Locate and identify every blood parasite.
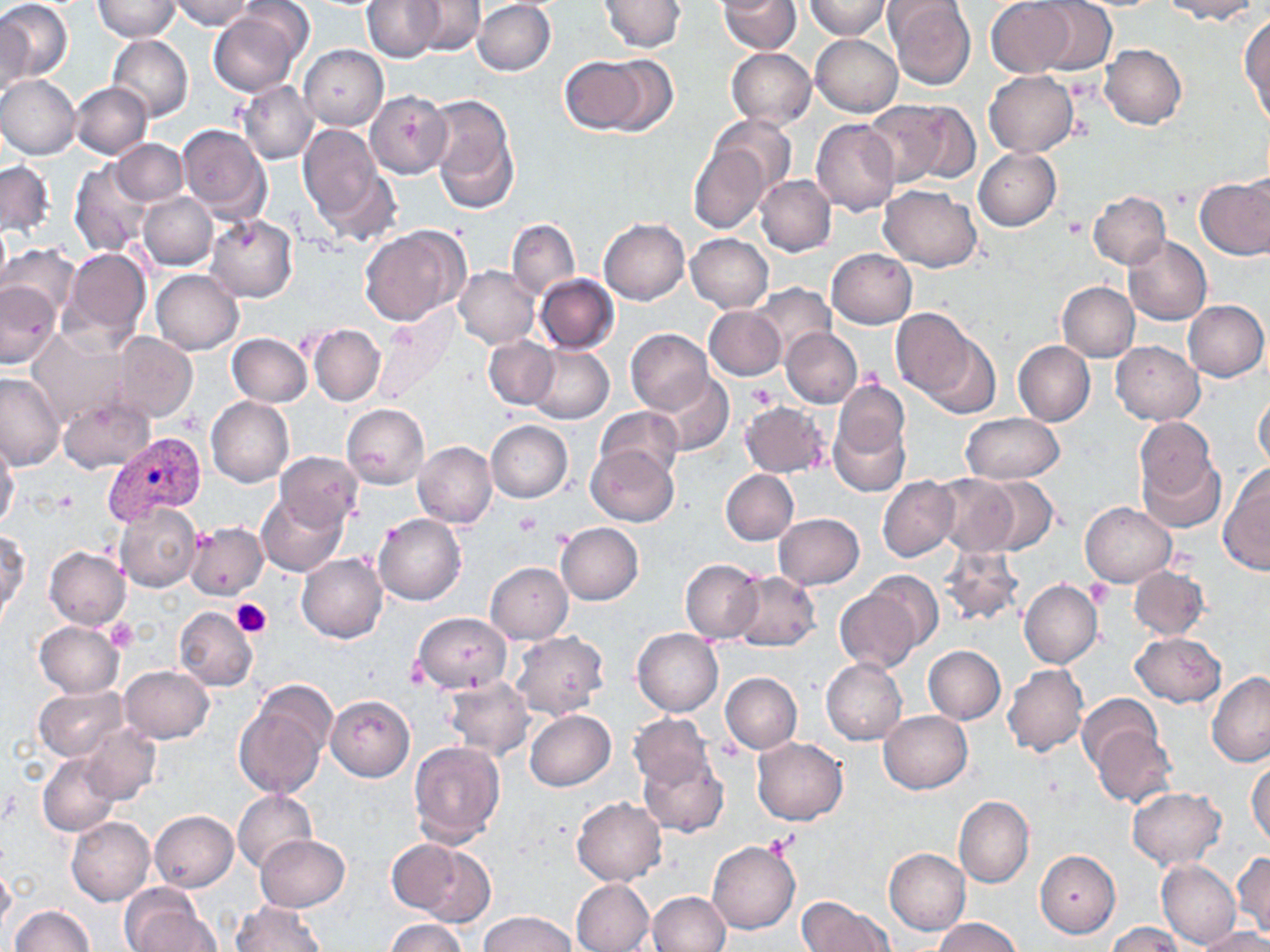
Approximate bounding boxes as [x1, y1, x2, y2] in pixels.
Plasmodium vivax-infected red blood cells: [102, 433, 207, 524].
No Plasmodium falciparum, Plasmodium ovale, Plasmodium malariae, Babesia divergens, or Trypanosoma brucei observed.

Platelet locations: [1063, 215, 1086, 238], [856, 364, 882, 389], [749, 385, 779, 412], [513, 511, 540, 536], [1085, 580, 1114, 608], [231, 597, 271, 638], [104, 619, 138, 652]. Uninfected red blood cell locations: [0, 0, 72, 82], [169, 0, 253, 30], [362, 0, 443, 61], [409, 0, 483, 56], [598, 0, 685, 52], [716, 0, 801, 53], [804, 0, 890, 39], [885, 0, 976, 90], [1163, 0, 1260, 22], [94, 1, 179, 41], [472, 1, 556, 76], [1028, 1, 1116, 73], [986, 2, 1078, 77], [589, 9, 684, 93], [0, 10, 35, 102], [209, 10, 304, 97], [1240, 16, 1269, 120], [107, 34, 193, 122], [811, 34, 902, 117], [298, 44, 388, 130], [1100, 44, 1187, 129], [726, 48, 816, 128], [596, 54, 678, 138], [559, 56, 652, 134], [984, 71, 1079, 156], [1, 74, 81, 159], [238, 80, 319, 165], [70, 82, 152, 160], [364, 91, 452, 178], [423, 94, 521, 213], [861, 100, 954, 189], [900, 102, 984, 184], [709, 115, 795, 195], [810, 119, 900, 217], [297, 121, 393, 231], [177, 123, 271, 221], [112, 140, 186, 206], [689, 145, 769, 233], [974, 148, 1061, 230], [1, 160, 53, 237], [69, 160, 153, 256], [756, 175, 836, 256], [1196, 177, 1270, 259], [877, 184, 982, 271], [1088, 192, 1171, 268], [138, 193, 217, 270], [204, 214, 299, 302], [507, 218, 579, 299], [598, 218, 689, 304], [0, 220, 11, 298], [361, 226, 469, 325], [686, 233, 772, 312], [1123, 237, 1211, 324], [2, 245, 80, 324], [60, 247, 150, 349], [827, 248, 916, 328], [455, 265, 538, 348], [151, 270, 243, 355], [535, 274, 619, 353], [0, 281, 61, 368], [750, 282, 835, 362], [1057, 282, 1140, 361], [1183, 300, 1269, 382], [705, 306, 786, 381], [891, 309, 974, 400], [371, 313, 458, 407], [309, 324, 384, 406], [911, 326, 999, 419], [626, 328, 715, 415], [781, 328, 862, 408], [27, 329, 129, 424], [111, 332, 198, 424], [228, 333, 313, 406], [484, 336, 558, 409], [1013, 340, 1095, 426], [1111, 340, 1204, 424], [525, 344, 613, 424], [0, 372, 67, 472], [653, 372, 733, 455], [832, 380, 909, 460], [1253, 389, 1270, 472], [58, 395, 154, 472], [206, 396, 294, 487], [740, 402, 829, 477], [342, 403, 429, 489], [595, 406, 682, 480], [960, 413, 1065, 484], [1134, 417, 1221, 517], [828, 418, 910, 498], [486, 420, 572, 502], [0, 439, 20, 532], [413, 441, 497, 529], [585, 445, 678, 526], [274, 452, 362, 529], [1219, 464, 1270, 575], [721, 469, 798, 545], [930, 473, 1020, 556], [878, 476, 958, 562], [976, 476, 1058, 556], [258, 492, 350, 577], [1081, 502, 1176, 587], [115, 503, 203, 592], [773, 513, 865, 589], [374, 514, 466, 605], [185, 522, 268, 600], [555, 523, 644, 605], [0, 530, 29, 619], [940, 545, 1022, 626], [44, 546, 131, 630], [297, 553, 388, 644], [679, 560, 763, 644], [485, 562, 573, 643], [1129, 565, 1210, 641], [861, 569, 944, 653], [728, 571, 821, 651], [1019, 579, 1101, 668], [833, 581, 929, 674], [173, 606, 257, 691], [412, 612, 510, 692], [34, 621, 125, 697], [633, 628, 723, 716], [511, 631, 608, 721], [1132, 632, 1225, 708], [923, 646, 1006, 724], [821, 658, 907, 746], [1003, 663, 1088, 757], [119, 665, 214, 743], [721, 672, 801, 754], [1207, 673, 1270, 766], [442, 675, 534, 761], [34, 687, 128, 762], [1078, 693, 1162, 775], [327, 695, 414, 781], [233, 696, 330, 797], [525, 710, 616, 791], [878, 710, 972, 794], [629, 713, 713, 791], [1087, 720, 1176, 807], [79, 725, 159, 804], [753, 738, 847, 824], [407, 740, 506, 845], [39, 752, 119, 836], [639, 752, 728, 837], [1248, 759, 1270, 848], [1127, 786, 1226, 869], [232, 788, 317, 875], [572, 796, 666, 885], [954, 796, 1033, 889], [150, 810, 238, 891], [66, 817, 155, 905], [255, 835, 349, 911], [386, 837, 485, 923], [708, 841, 800, 934], [884, 848, 970, 935], [1035, 851, 1120, 937], [1232, 852, 1270, 939], [1156, 859, 1240, 950], [0, 862, 15, 938], [571, 878, 654, 952], [119, 886, 212, 952], [646, 891, 730, 952], [797, 896, 893, 952], [233, 903, 326, 951], [10, 906, 94, 952], [479, 911, 577, 952], [932, 917, 1024, 952], [383, 919, 466, 952], [1107, 924, 1185, 952], [1197, 926, 1270, 951]. Slide-level diagnosis: Plasmodium vivax. One field of a larger specimen. May-Grünwald-Giemsa-stained preparation. Thin blood smear. Image is 1270×952 pixels. Captured at 1000x magnification. Optical microscopy.